Locate every Plasmodium falciparum-infected red blood cell.
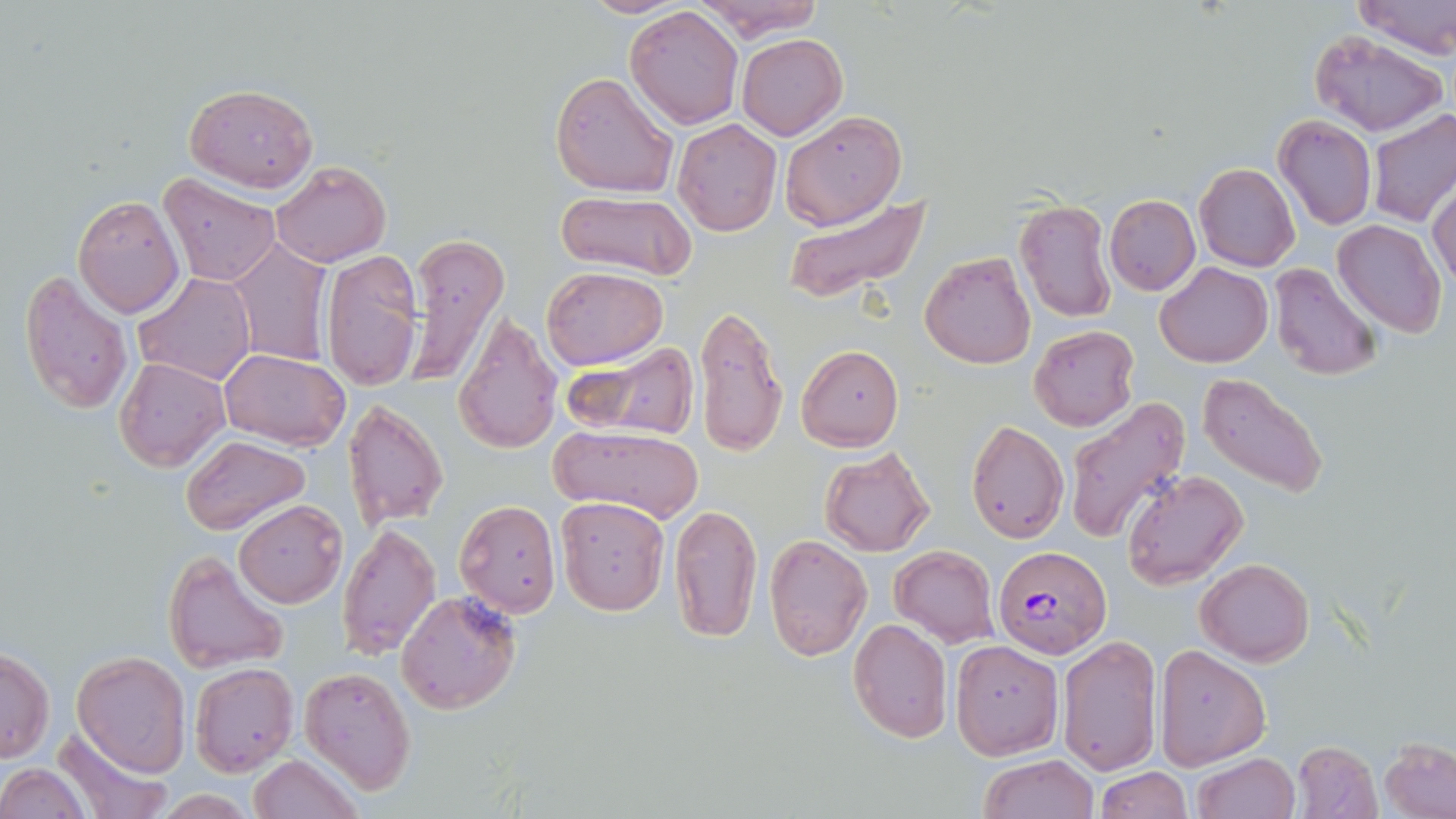
Approximate bounding boxes as named x1/y1/x2/y2 corners in pixels.
Plasmodium falciparum-infected red blood cells: (x1=993, y1=546, x2=1111, y2=657).

Uninfected red blood cell locations: (x1=577, y1=0, x2=694, y2=17), (x1=689, y1=0, x2=824, y2=39), (x1=1353, y1=0, x2=1456, y2=59), (x1=625, y1=7, x2=744, y2=129), (x1=1308, y1=30, x2=1447, y2=138), (x1=737, y1=34, x2=848, y2=140), (x1=550, y1=72, x2=679, y2=198), (x1=183, y1=83, x2=318, y2=193), (x1=1369, y1=109, x2=1456, y2=227), (x1=780, y1=110, x2=907, y2=229), (x1=1273, y1=116, x2=1377, y2=232), (x1=672, y1=118, x2=782, y2=236), (x1=270, y1=160, x2=390, y2=268), (x1=1193, y1=163, x2=1299, y2=272), (x1=159, y1=174, x2=282, y2=286), (x1=1428, y1=182, x2=1456, y2=293), (x1=786, y1=189, x2=929, y2=305), (x1=555, y1=190, x2=697, y2=279), (x1=1104, y1=194, x2=1200, y2=294), (x1=74, y1=195, x2=185, y2=318), (x1=1014, y1=200, x2=1116, y2=321), (x1=1334, y1=219, x2=1446, y2=337), (x1=403, y1=234, x2=509, y2=385), (x1=228, y1=241, x2=333, y2=367), (x1=322, y1=249, x2=423, y2=392), (x1=919, y1=250, x2=1036, y2=369), (x1=1155, y1=263, x2=1272, y2=367), (x1=1271, y1=264, x2=1381, y2=381), (x1=542, y1=266, x2=667, y2=369), (x1=19, y1=269, x2=134, y2=416), (x1=134, y1=273, x2=255, y2=385), (x1=694, y1=302, x2=789, y2=459), (x1=452, y1=312, x2=564, y2=455), (x1=1030, y1=325, x2=1138, y2=431), (x1=566, y1=342, x2=701, y2=442), (x1=796, y1=344, x2=903, y2=451), (x1=219, y1=349, x2=349, y2=451), (x1=115, y1=357, x2=230, y2=472), (x1=1197, y1=372, x2=1329, y2=499), (x1=342, y1=398, x2=448, y2=529), (x1=1064, y1=399, x2=1190, y2=542), (x1=966, y1=419, x2=1067, y2=542), (x1=552, y1=424, x2=704, y2=525), (x1=181, y1=436, x2=312, y2=534), (x1=820, y1=446, x2=936, y2=557), (x1=1121, y1=470, x2=1249, y2=590), (x1=555, y1=497, x2=671, y2=616), (x1=233, y1=499, x2=347, y2=607), (x1=455, y1=499, x2=561, y2=616), (x1=668, y1=503, x2=762, y2=643), (x1=338, y1=521, x2=440, y2=658), (x1=763, y1=534, x2=873, y2=661), (x1=890, y1=545, x2=999, y2=646), (x1=164, y1=550, x2=290, y2=672), (x1=1197, y1=558, x2=1314, y2=666), (x1=397, y1=590, x2=521, y2=715), (x1=847, y1=618, x2=953, y2=742), (x1=1058, y1=635, x2=1162, y2=775), (x1=949, y1=639, x2=1063, y2=759), (x1=1154, y1=645, x2=1269, y2=768), (x1=0, y1=648, x2=53, y2=764), (x1=72, y1=650, x2=191, y2=777), (x1=190, y1=662, x2=298, y2=777), (x1=299, y1=666, x2=417, y2=793), (x1=53, y1=726, x2=173, y2=819), (x1=1381, y1=739, x2=1455, y2=818), (x1=1292, y1=741, x2=1383, y2=819), (x1=1191, y1=752, x2=1300, y2=819), (x1=249, y1=753, x2=363, y2=819), (x1=979, y1=754, x2=1098, y2=819), (x1=0, y1=763, x2=92, y2=818), (x1=1096, y1=767, x2=1191, y2=819), (x1=150, y1=792, x2=263, y2=819). Slide-level diagnosis: Plasmodium falciparum. Captured at 1000x magnification. Thin blood smear. May-Grünwald-Giemsa stain. Image is 1456×819 pixels. Single field of view. Light microscopy.